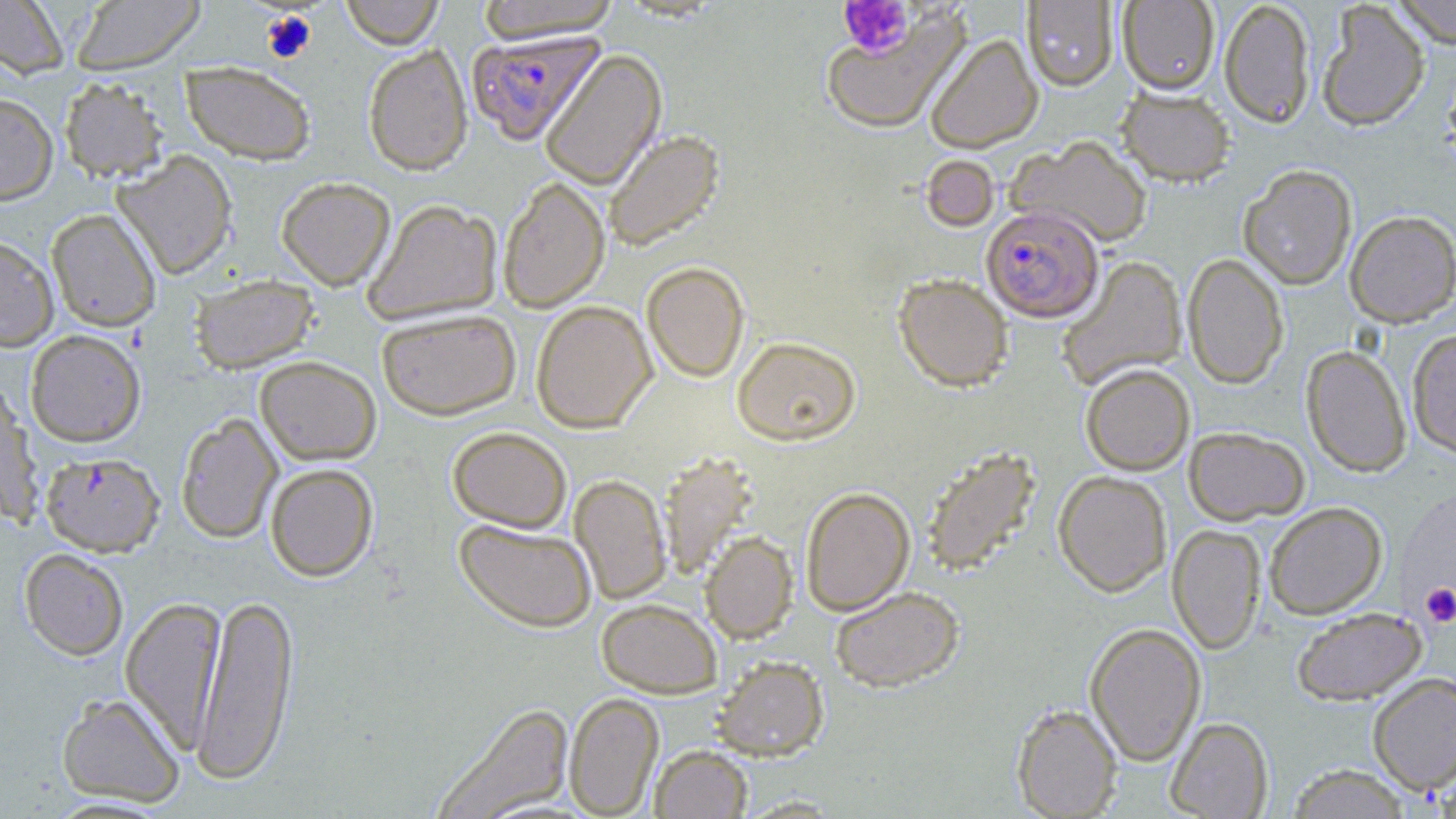

Summary:
  - Coordinate format: approximate bounding boxes as [x1, y1, x2, y2] in pixels
  - Platelet locations: [838, 0, 915, 57], [261, 11, 317, 63], [1410, 548, 1455, 633], [1421, 583, 1456, 627]
  - Plasmodium falciparum-infected red blood cell locations: [466, 31, 603, 145], [981, 205, 1104, 322], [41, 451, 165, 556]
  - Uninfected red blood cell locations: [0, 0, 70, 79], [340, 0, 444, 49], [1117, 0, 1220, 95], [1219, 0, 1316, 128], [1391, 0, 1455, 47], [70, 1, 206, 74], [476, 1, 622, 42], [1022, 1, 1118, 91], [1316, 1, 1430, 132], [820, 6, 968, 135], [925, 33, 1043, 153], [363, 44, 473, 175], [540, 49, 666, 190], [181, 61, 317, 165], [1443, 63, 1456, 165], [59, 76, 169, 183], [1117, 86, 1235, 187], [0, 92, 58, 205], [603, 129, 724, 252], [1008, 135, 1153, 249], [112, 151, 238, 279], [921, 154, 1000, 232], [1238, 164, 1358, 290], [276, 176, 396, 290], [498, 176, 610, 313], [362, 198, 503, 324], [46, 208, 162, 332], [1345, 210, 1456, 327], [0, 235, 59, 352], [1182, 253, 1289, 389], [1056, 255, 1187, 391], [641, 260, 750, 383], [893, 273, 1013, 392], [189, 274, 318, 373], [531, 299, 657, 434], [377, 309, 521, 420], [1407, 328, 1456, 459], [25, 330, 146, 447], [732, 336, 861, 446], [1301, 344, 1412, 478], [254, 356, 381, 465], [1080, 364, 1195, 475], [0, 385, 44, 528], [175, 412, 284, 544], [447, 426, 572, 532], [1184, 426, 1310, 525], [921, 444, 1041, 577], [657, 451, 759, 580], [265, 463, 378, 581], [1053, 470, 1172, 597], [569, 474, 671, 605], [799, 486, 915, 616], [1265, 502, 1387, 619], [455, 519, 597, 632], [1168, 524, 1266, 655], [700, 531, 798, 642], [19, 548, 129, 660], [829, 586, 964, 692], [194, 591, 298, 786], [120, 595, 227, 753], [596, 598, 722, 698], [1292, 607, 1426, 705], [1085, 622, 1206, 765], [712, 655, 829, 761], [1368, 672, 1456, 794], [57, 692, 185, 807], [564, 692, 664, 817], [432, 702, 575, 818], [1012, 703, 1122, 818], [1165, 716, 1273, 818], [649, 744, 753, 819], [1286, 763, 1411, 818], [736, 795, 846, 817]
  - Slide-level diagnosis: Plasmodium falciparum
  - Stain: May-Grünwald-Giemsa
  - Preparation: thin blood smear
  - Image size: 1456×819 pixels
  - Magnification: 1000x
  - Modality: optical microscopy
  - Field of view: one of a larger specimen